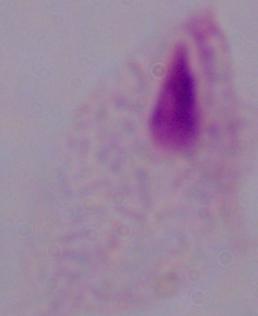 Captured at 1000x magnification. Micrograph. A trichomonad is seen.